Assess this cell for malaria.
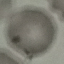
It is uninfected.

Summary:
  - Stain: Giemsa
  - Image type: automatically extracted cell patch, resized to 64 × 64 pixels
  - Capture: smartphone camera at the microscope eyepiece
  - Preparation: thin blood smear